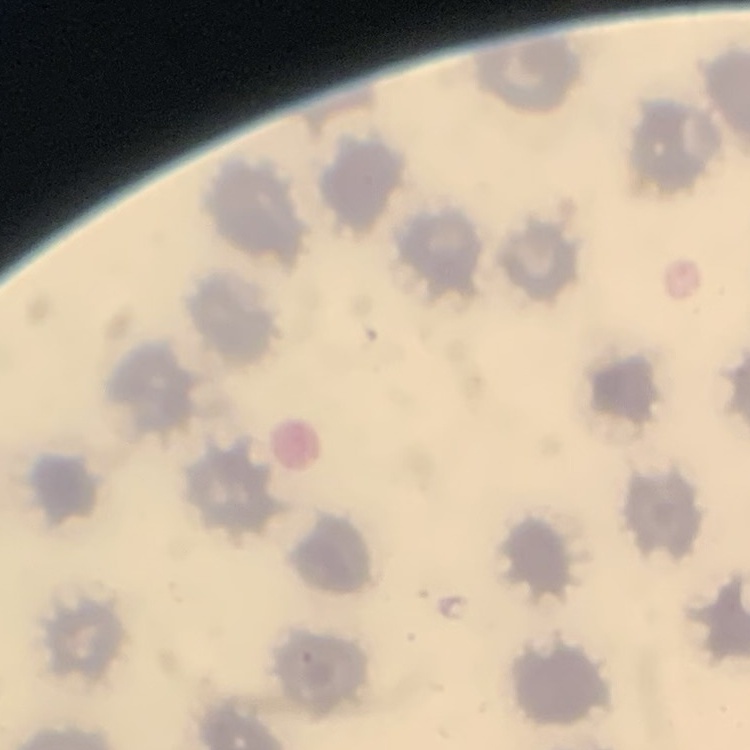

Summary:
  - Erythrocyte morphology: no rouleaux formation
  - Preparation: thin blood film
  - Image type: square crop of a larger photomicrograph
  - Stain: Field's or Giemsa